Classify this cell by malaria status.
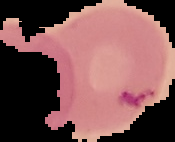

Uninfected.

Image is 175×142 pixels. Segmented cell region on a black background. From a thin blood smear.